Assess this cell for malaria.
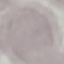

Uninfected.

Summary:
  - Image type: automatically extracted cell patch, resized to 64 × 64 pixels
  - Preparation: thin smear
  - Capture: smartphone through the microscope eyepiece
  - Stain: Giemsa